Point out each malaria parasite.
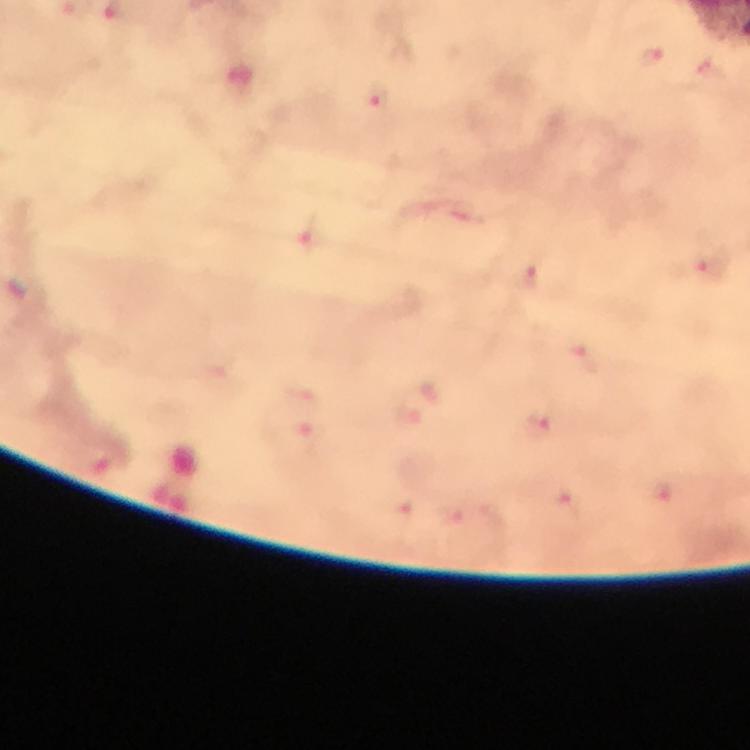

Approximate centers as [x, y] in pixels.
Malaria parasites: [652, 56], [238, 83], [381, 103], [699, 269], [530, 279], [583, 357], [411, 421], [545, 423], [661, 493], [565, 499], [397, 513], [450, 514].

cropped from = a single field of view
context = from a malaria diagnostic workup
stain = Giemsa
magnification = 100x
capture = smartphone photograph through a microscope
preparation = thick smear
image size = 750×750 pixels
immersion oil = applied